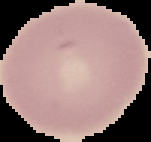 Image is 151×142 pixels. The area outside the segmented cell region is set to black. Malaria status: uninfected. From a thin blood smear.